State which parasite is depicted.
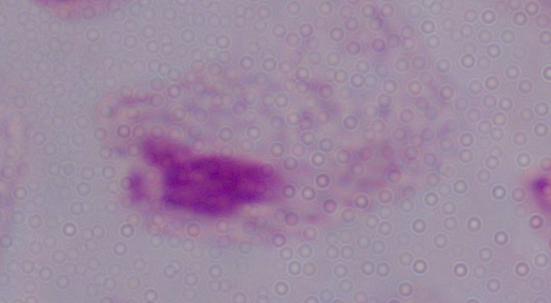
This is a trichomonad.

Summary:
  - Magnification: 1000x
  - Modality: photomicrograph